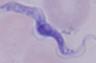 Captured at 1000x magnification. Micrograph. A trypanosome is shown.